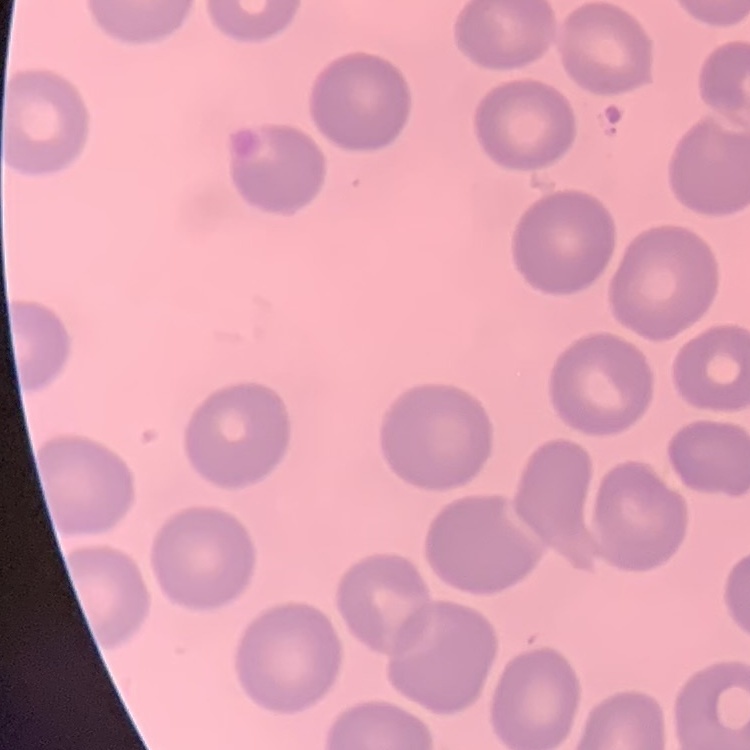
Summary:
  - Erythrocyte morphology: no rouleaux formation
  - Image type: square crop of a larger photomicrograph
  - Preparation: thin blood film
  - Stain: Field's or Giemsa